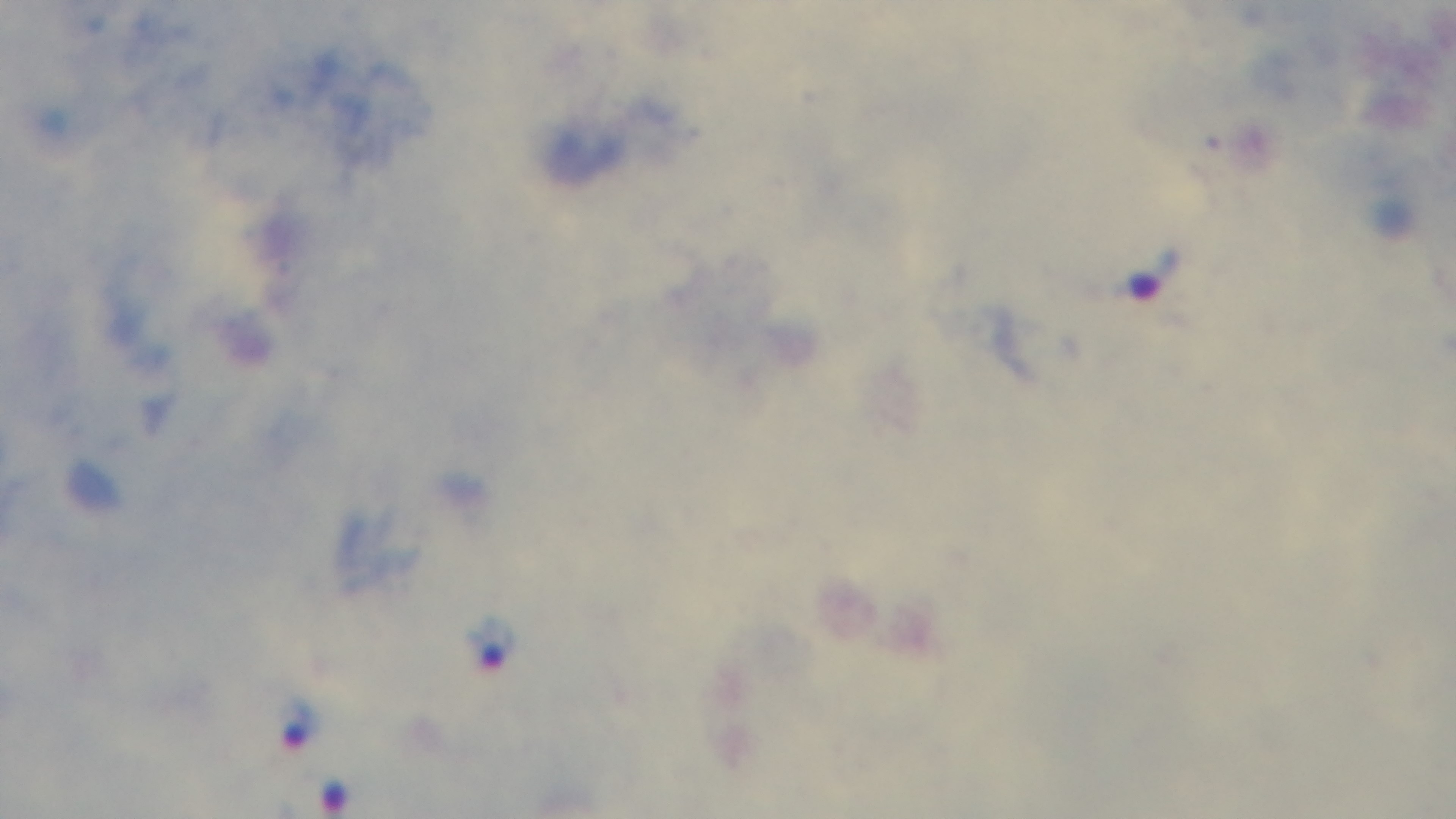 Preparation: thick smear. 100x oil-immersion objective. One field from the slide. Photomicrograph. Mounted 4K digital camera. Malaria status: infected. Giemsa stain.